Locate every leukocyte (white blood cell).
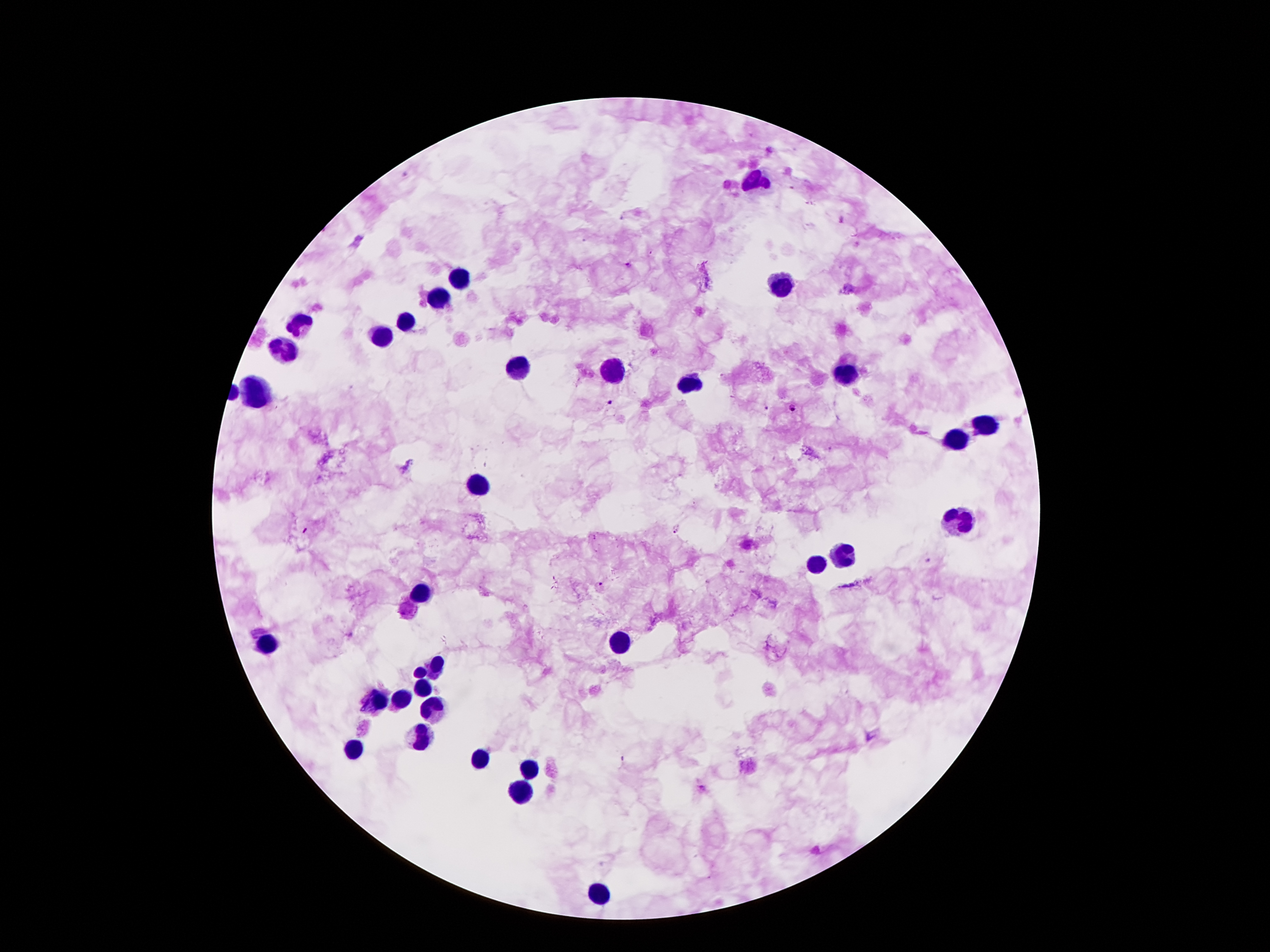

Approximate centers as {x, y} in pixels.
Leukocytes: {758, 180}, {462, 278}, {783, 280}, {437, 293}, {305, 323}, {407, 323}, {384, 335}, {283, 349}, {521, 367}, {615, 371}, {842, 377}, {691, 385}, {256, 394}, {981, 425}, {956, 442}, {477, 484}, {958, 521}, {842, 557}, {815, 564}, {420, 593}, {617, 644}, {265, 645}, {435, 665}, {420, 672}, {424, 688}, {399, 697}, {372, 701}, {433, 705}, {422, 738}, {355, 745}, {481, 756}, {527, 768}, {523, 793}, {596, 891}.

Summary:
  - Plasmodium parasite locations: {843, 220}, {629, 266}, {608, 403}, {766, 407}, {792, 407}, {676, 528}, {306, 529}, {927, 560}, {600, 583}, {703, 787}
  - Capture: smartphone camera through the microscope eyepiece
  - Stain: Giemsa
  - Field of view: one from this slide
  - Magnification: 100x
  - Patient malaria status: infected with Plasmodium falciparum
  - Preparation: thick peripheral-blood smear
  - Image size: 1270×952 pixels